Identify the preparation type.
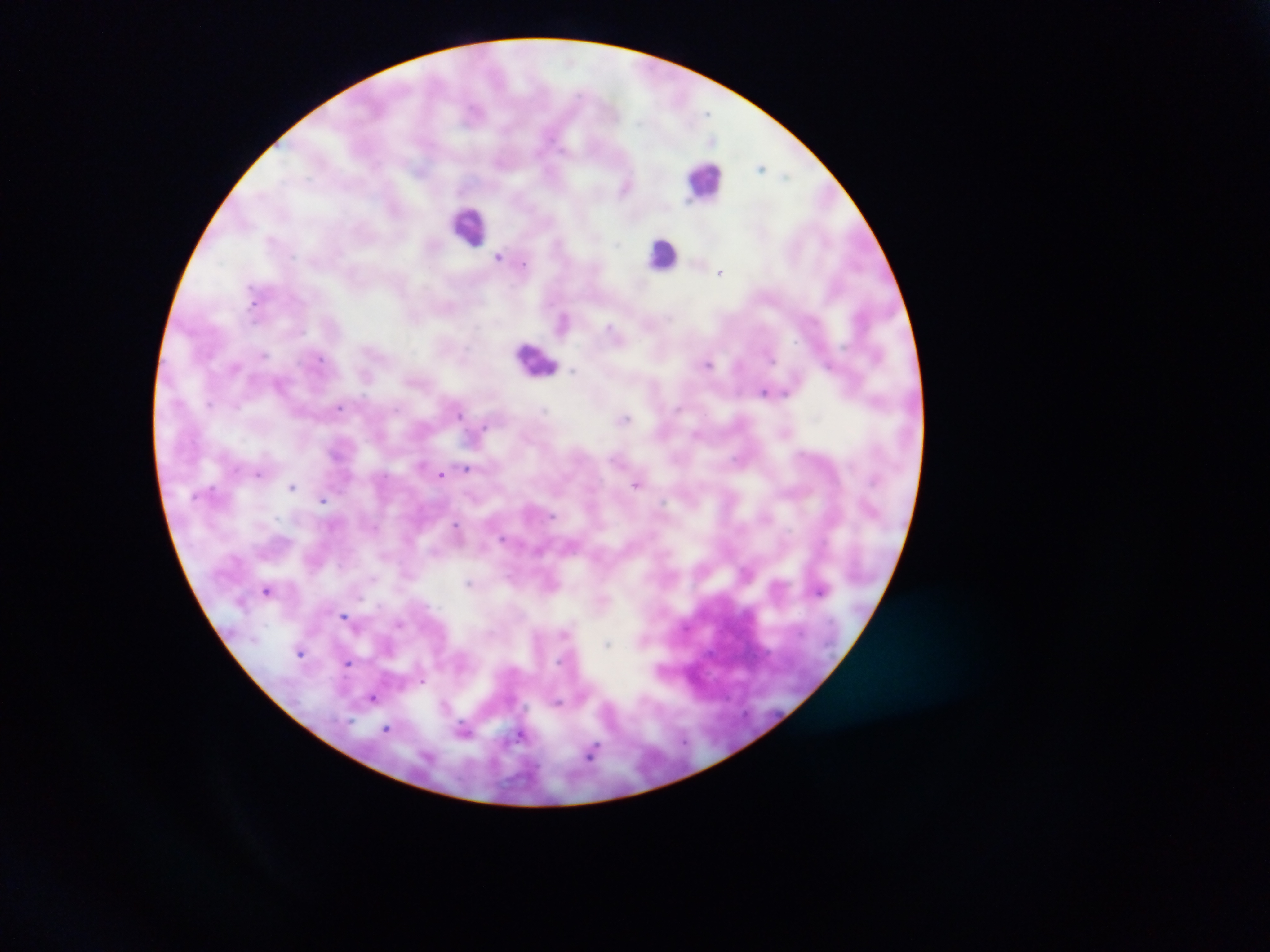
Thick blood smear.

{
  "image_size": "1270×952 pixels",
  "malaria_parasite_locations": "approximate centers as x y in pixels: 761 167; 627 186; 500 256; 720 272; 564 320; 708 363; 830 365; 765 391; 339 406; 624 418; 466 468; 258 473; 442 474; 637 483; 292 485; 323 499; 458 530; 471 583; 268 590; 345 615; 400 622; 608 645; 300 651; 348 663; 423 680; 373 698; 558 702; 386 728; 464 730; 522 733; 592 753",
  "field_of_view": "single",
  "leukocyte_locations": "approximate centers as x y in pixels: 705 180; 469 226; 663 253; 537 359",
  "capture": "mobile-phone photograph through a microscope",
  "country": "Ghana"
}